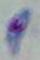

{
  "identification": "Toxoplasma gondii",
  "modality": "micrograph",
  "magnification": "1000x"
}